Identify the preparation type.
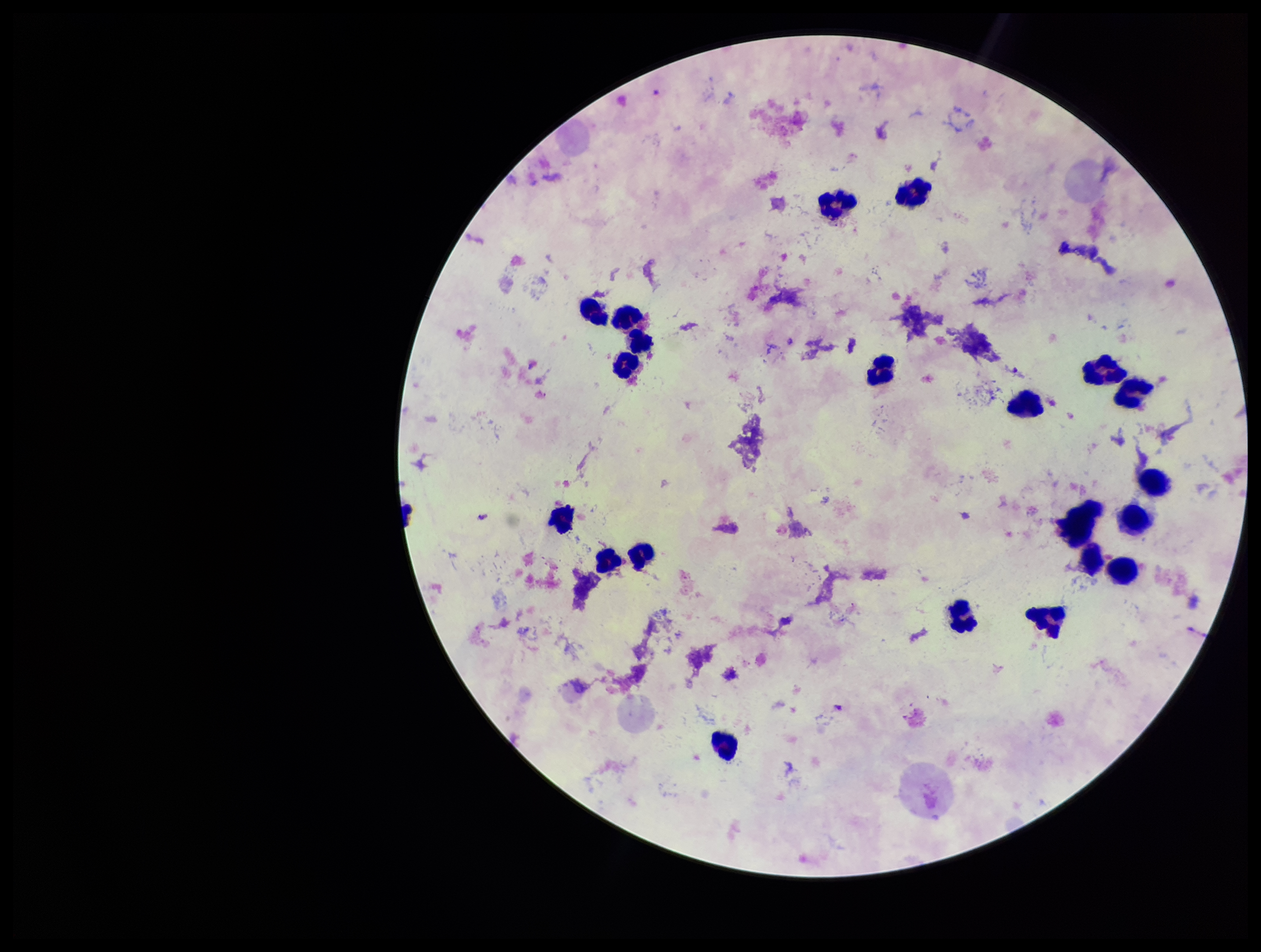
A thick smear.

Summary:
  - Plasmodium parasites: none identified
  - Capture: smartphone photograph through the microscope eyepiece
  - Leukocyte count: 23
  - Patient malaria status: positive
  - Species reported for this patient: Plasmodium falciparum
  - Parasite count: 0
  - Stain: Giemsa
  - Field of view: single
  - Image size: 1261×952 pixels